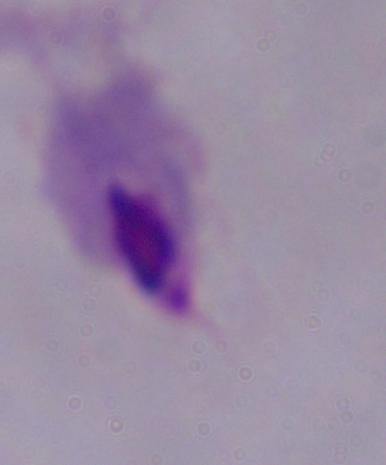

Summary:
  - Modality: micrograph
  - Identification: trichomonad
  - Magnification: 1000x